Assess this cell for malaria.
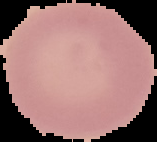
It is uninfected.

From a thin blood smear. Cell region segmented out of the field of view; the surrounding area is masked to black. Image is 157×142 pixels.